Classify this cell by malaria status.
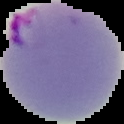
It is parasitized.

From a thin blood smear. Image is 124×124 pixels. Cell region segmented out of the field of view; the surrounding area is masked to black.